Assess the morphology of the erythrocytes.
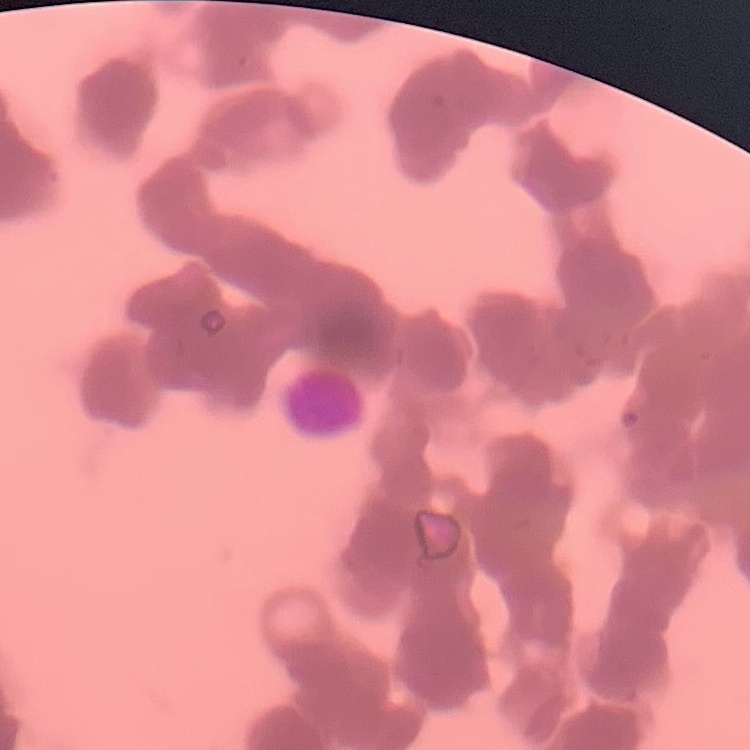

Rouleaux formation.

Summary:
  - Image type: one tile cut from a larger photomicrograph
  - Stain: Field's or Giemsa
  - Preparation: thin blood smear